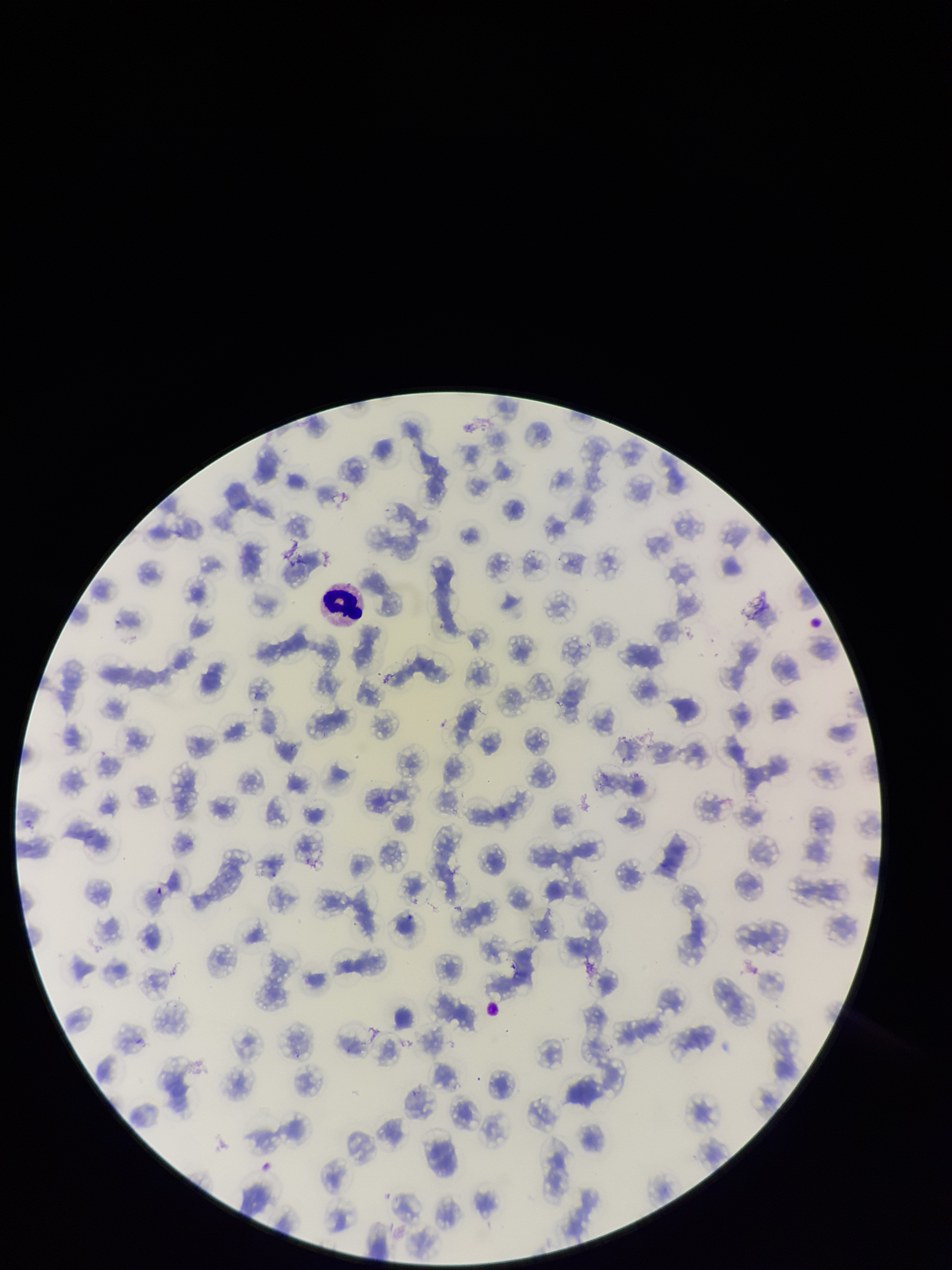

Summary:
  - Patient malaria status: positive
  - Field of view: single
  - Parasitized red blood cells: none identified
  - Capture: smartphone photograph through the microscope eyepiece
  - Preparation: thin
  - Stain: Giemsa
  - Red blood cell count: 139
  - Species reported for this patient: Plasmodium falciparum
  - Image size: 952×1270 pixels
  - Parasitized red blood cell count: 0